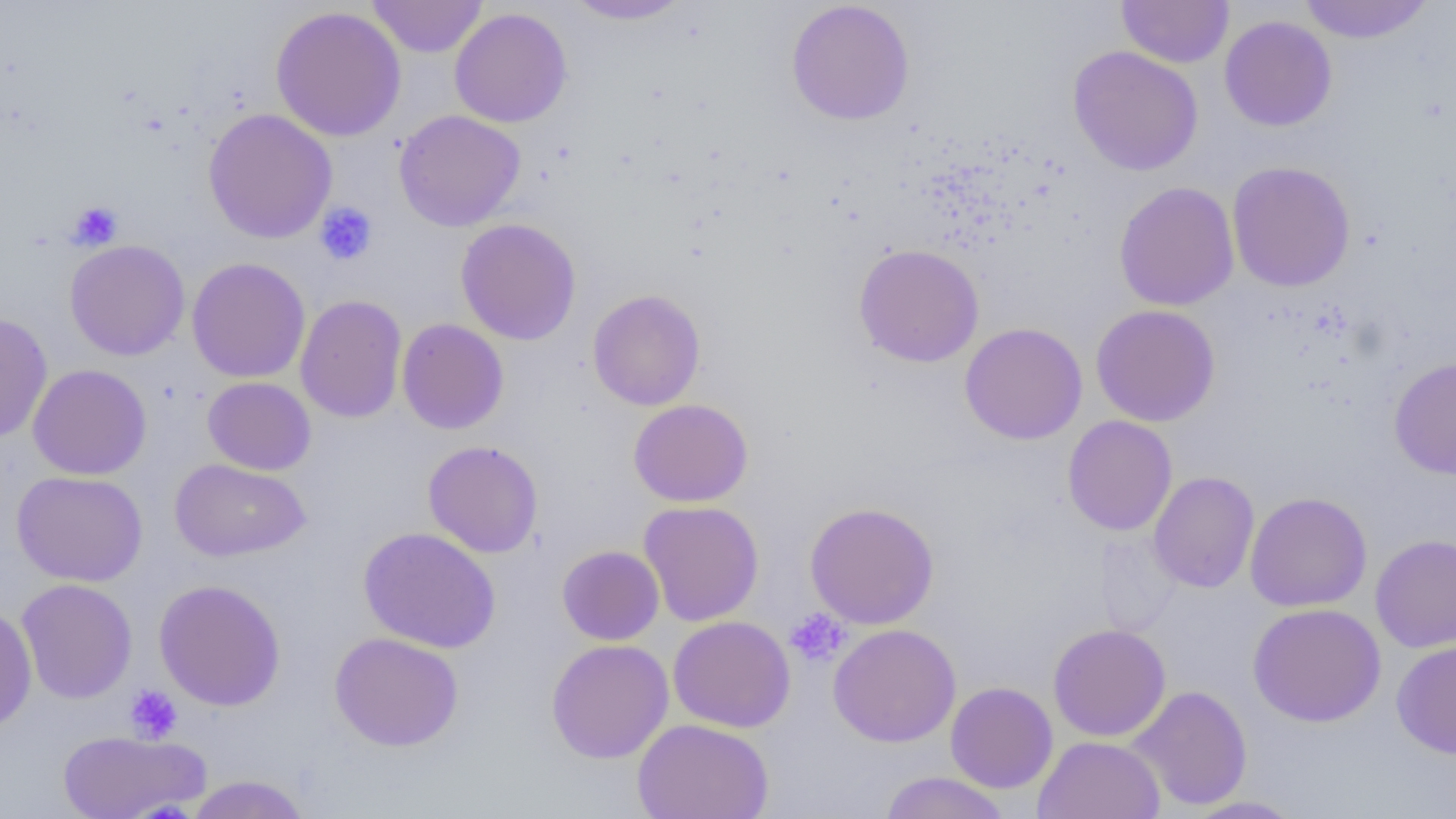

slide_level_diagnosis: negative for blood parasites
modality: light microscopy
magnification: 1000x
preparation: thin blood smear
uninfected_red_blood_cell_locations: 'approximate bounding boxes as (x1, y1, x2, y2) in pixels: (367, 0, 487, 58), (562, 0, 694, 25), (1116, 0, 1234, 68), (1298, 0, 1435, 44), (786, 1, 915, 126), (270, 6, 407, 142), (449, 7, 573, 128), (1219, 15, 1337, 131), (1067, 45, 1204, 176), (203, 108, 337, 244), (394, 109, 525, 231), (1226, 160, 1356, 292), (1114, 181, 1240, 311), (456, 218, 581, 345), (65, 240, 190, 361), (853, 243, 985, 367), (187, 257, 311, 383), (587, 289, 706, 411), (295, 294, 408, 423), (1091, 304, 1221, 427), (0, 311, 53, 443), (397, 318, 509, 434), (959, 322, 1088, 445), (1389, 355, 1456, 479), (28, 363, 152, 480), (202, 377, 316, 475), (628, 398, 753, 507), (1062, 415, 1178, 536), (423, 440, 543, 558), (170, 459, 311, 562), (11, 470, 148, 587), (1148, 471, 1259, 593), (1245, 491, 1372, 612), (638, 501, 764, 626), (804, 501, 940, 630), (358, 526, 501, 653), (1370, 534, 1456, 653), (557, 545, 665, 645), (16, 578, 138, 704), (154, 579, 287, 711), (0, 603, 37, 733), (1247, 603, 1386, 727), (667, 615, 796, 733), (828, 623, 962, 747), (1048, 623, 1171, 741), (329, 632, 464, 752), (1391, 638, 1456, 759), (546, 639, 674, 763), (945, 681, 1058, 793), (1127, 685, 1253, 811), (632, 718, 774, 819), (58, 728, 209, 819), (1033, 735, 1165, 819), (878, 771, 1012, 819), (184, 775, 312, 819), (1181, 795, 1307, 818)'
field_of_view: one of a larger specimen
platelet_locations: 'approximate bounding boxes as (x1, y1, x2, y2) in pixels: (67, 201, 123, 251), (314, 201, 378, 266), (785, 608, 850, 666), (124, 685, 183, 744)'
image_size: 1456×819 pixels